Report the malaria status.
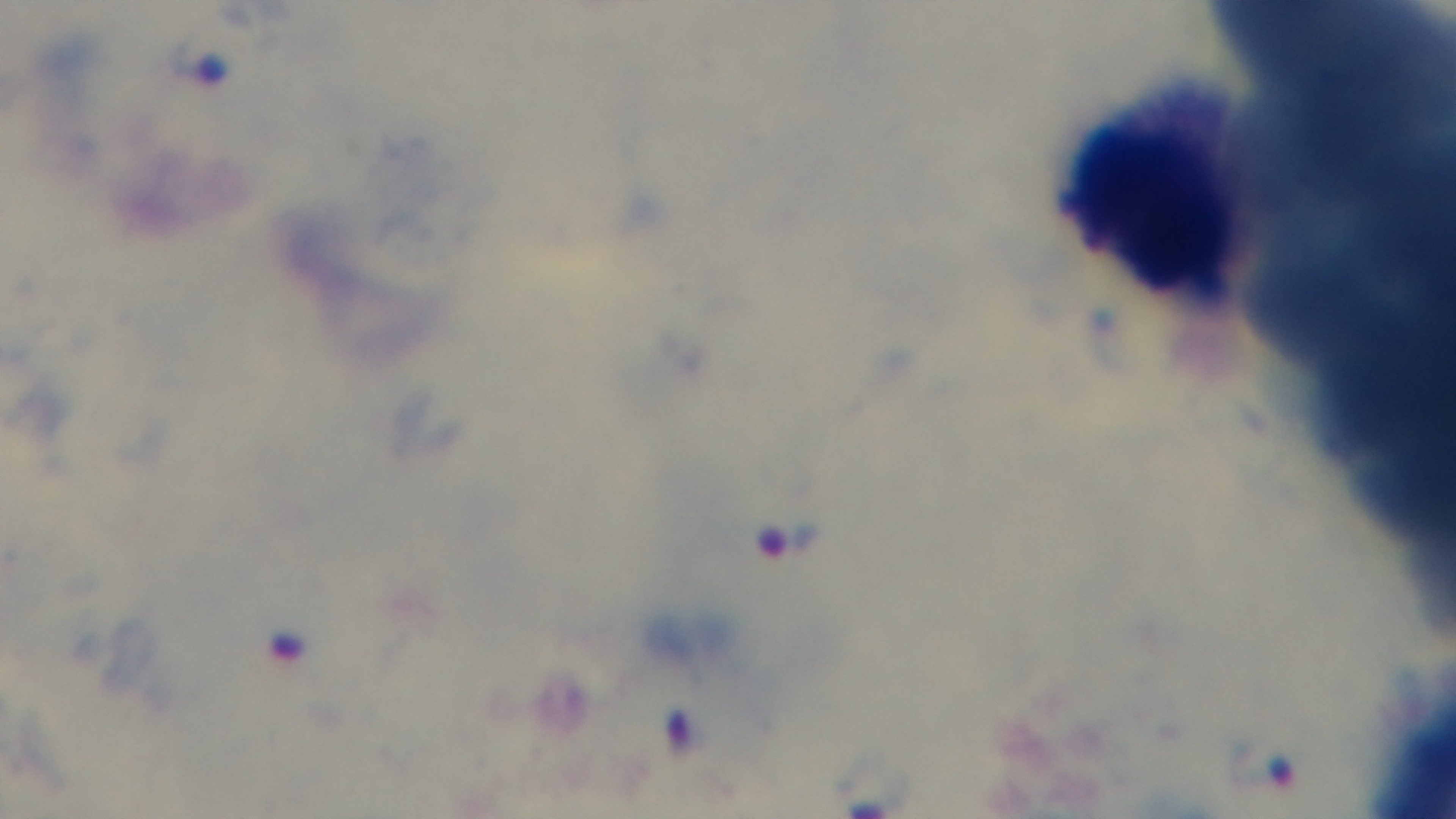

Infected.

objective: 100x oil immersion
field_of_view: one from the slide
stain: Giemsa
capture: mounted 4K digital camera
modality: light microscopy
preparation: thick